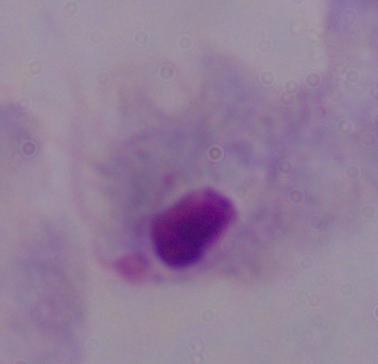
1000x magnification. Micrograph. A trichomonad is seen.